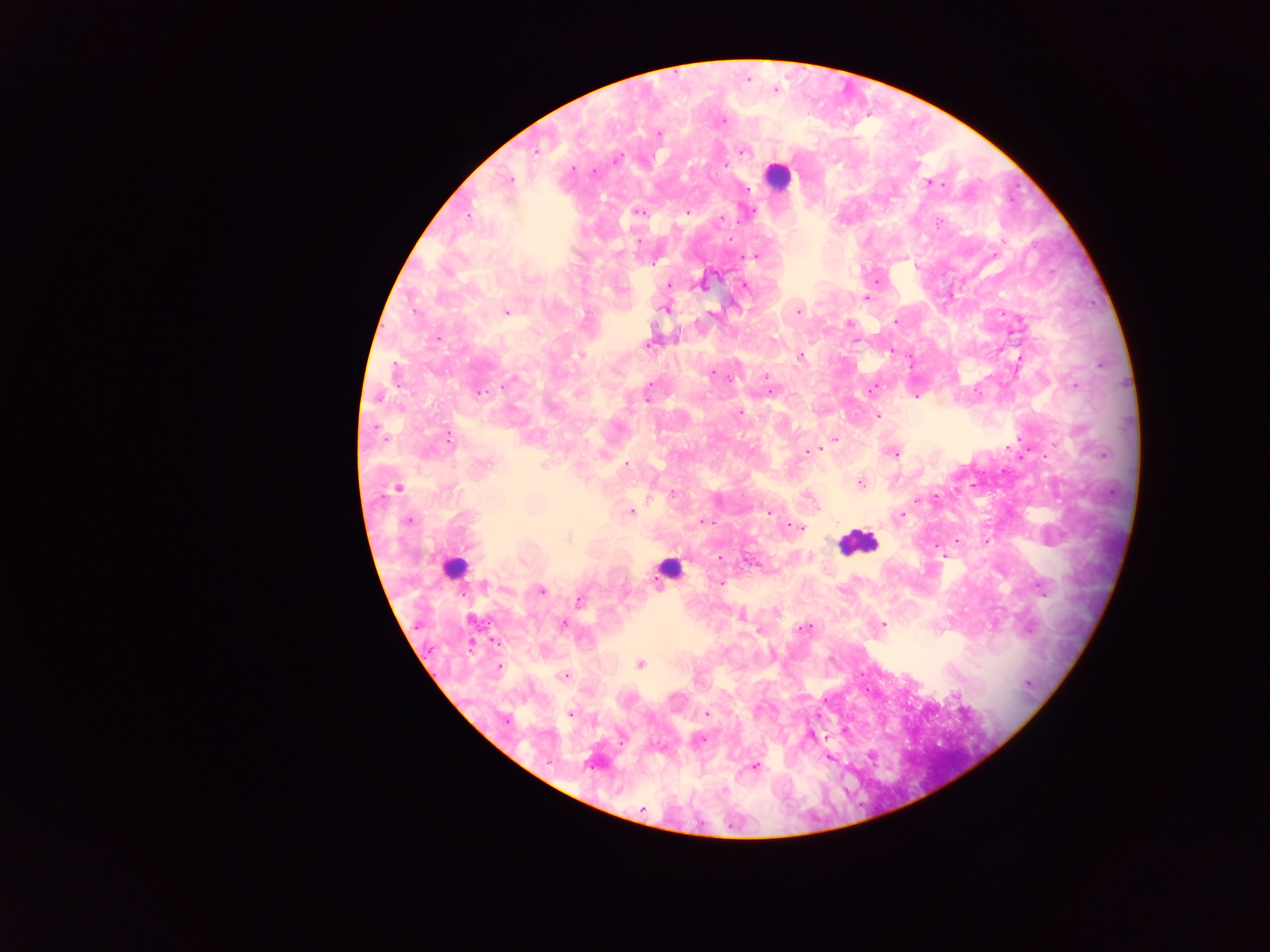

Approximate centers as x y in pixels.
Summary:
  - Malaria parasite locations: 774 90; 720 121; 658 133; 742 151; 615 160; 508 179; 930 183; 687 211; 639 212; 720 219; 638 242; 757 255; 877 280; 669 284; 743 286; 867 298; 666 309; 797 311; 506 312; 712 313; 894 321; 848 323; 439 337; 853 339; 648 343; 891 351; 581 354; 799 355; 712 373; 766 376; 871 388; 478 391; 770 392; 915 395; 648 397; 878 415; 834 439; 817 450; 808 452; 893 452; 627 464; 483 465; 860 482; 398 487; 672 493; 917 501; 767 510; 630 511; 900 516; 407 520; 702 521; 799 528; 985 541; 936 546; 719 558; 719 582; 1040 586; 540 590; 579 601; 740 614; 563 624; 882 624; 803 628; 639 664; 499 667; 564 676; 569 714; 706 714; 810 735; 698 739; 871 755; 829 757; 592 762; 755 766; 642 809
  - Leukocyte locations: 776 176; 856 542; 456 566; 669 569
  - Country: Ghana
  - Capture: mobile-phone photograph through a microscope
  - Image size: 1270×952 pixels
  - Preparation: thick blood smear
  - Field of view: single